Outline each blood parasite and name the species.
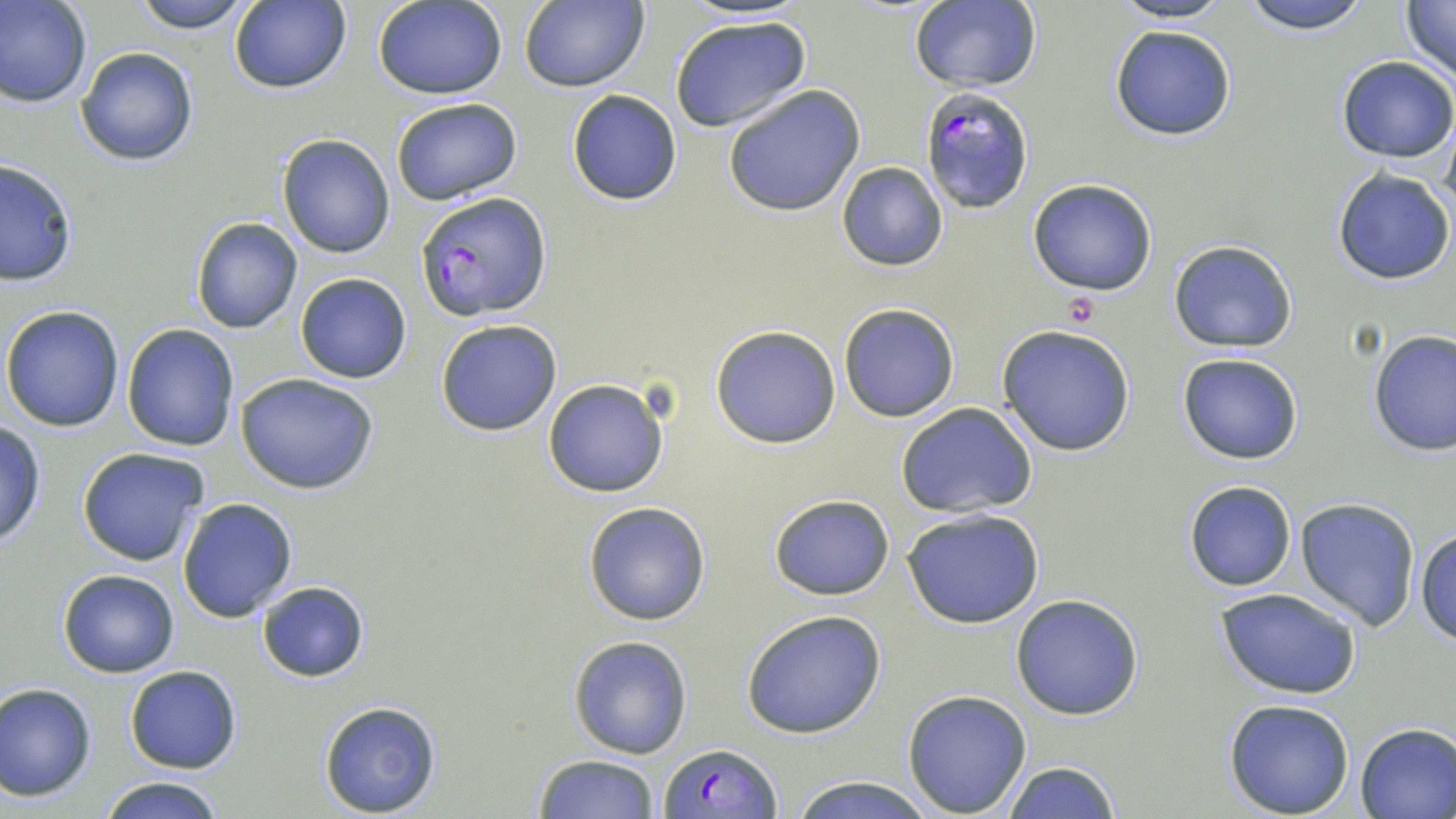

Approximate bounding boxes as [x1, y1, x2, y2] in pixels.
Plasmodium falciparum-infected red blood cells: [918, 89, 1035, 213], [418, 191, 552, 322], [660, 743, 779, 819].
No Plasmodium ovale, Plasmodium malariae, Plasmodium vivax, Babesia divergens, or Trypanosoma brucei observed.

slide-level diagnosis = Plasmodium falciparum
modality = light microscopy
magnification = 1000x
uninfected red blood cell locations = approximate bounding boxes as [x1, y1, x2, y2] in pixels: [1, 0, 93, 107], [132, 0, 255, 33], [518, 0, 648, 92], [1238, 0, 1376, 33], [228, 1, 351, 94], [374, 1, 507, 99], [908, 1, 1042, 92], [1106, 1, 1239, 25], [1399, 2, 1455, 81], [668, 16, 813, 133], [1108, 23, 1237, 140], [77, 47, 198, 165], [1336, 56, 1456, 162], [722, 84, 864, 216], [566, 90, 681, 206], [390, 98, 523, 206], [276, 133, 396, 259], [0, 158, 77, 286], [837, 162, 949, 271], [1332, 169, 1455, 284], [1028, 178, 1160, 296], [190, 217, 302, 334], [1168, 239, 1297, 352], [295, 273, 412, 384], [838, 303, 959, 423], [2, 306, 125, 431], [435, 319, 562, 437], [122, 322, 239, 450], [997, 324, 1137, 457], [711, 326, 841, 447], [1367, 330, 1455, 457], [1177, 351, 1303, 465], [237, 374, 380, 495], [542, 379, 670, 498], [895, 401, 1038, 518], [0, 421, 47, 549], [76, 447, 209, 568], [1183, 480, 1297, 591], [768, 494, 895, 602], [177, 497, 298, 622], [1295, 497, 1420, 631], [583, 500, 713, 626], [902, 507, 1044, 629], [1414, 526, 1456, 644], [57, 569, 180, 677], [256, 582, 369, 683], [1213, 588, 1361, 701], [1010, 594, 1144, 719], [741, 609, 888, 739], [568, 636, 691, 759], [124, 665, 242, 774], [0, 682, 97, 802], [902, 689, 1033, 816], [1225, 698, 1356, 818], [318, 701, 443, 817], [1355, 722, 1456, 818], [533, 754, 660, 819], [999, 761, 1121, 818], [98, 775, 225, 819], [786, 775, 934, 818]
image size = 1456×819 pixels
preparation = thin blood smear
stain = May-Grünwald-Giemsa
platelet locations = approximate bounding boxes as [x1, y1, x2, y2] in pixels: [1062, 295, 1100, 327]
field of view = one of a larger specimen